Identify the parasite.
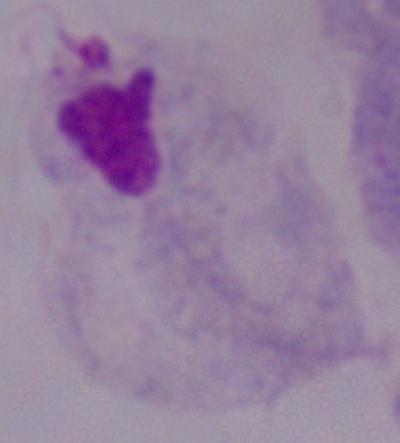
This is a trichomonad.

magnification = 1000x
modality = micrograph